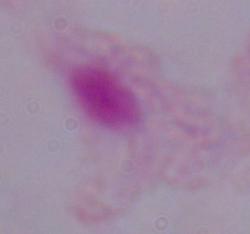

Summary:
  - Identification: trichomonad
  - Modality: photomicrograph
  - Magnification: 1000x